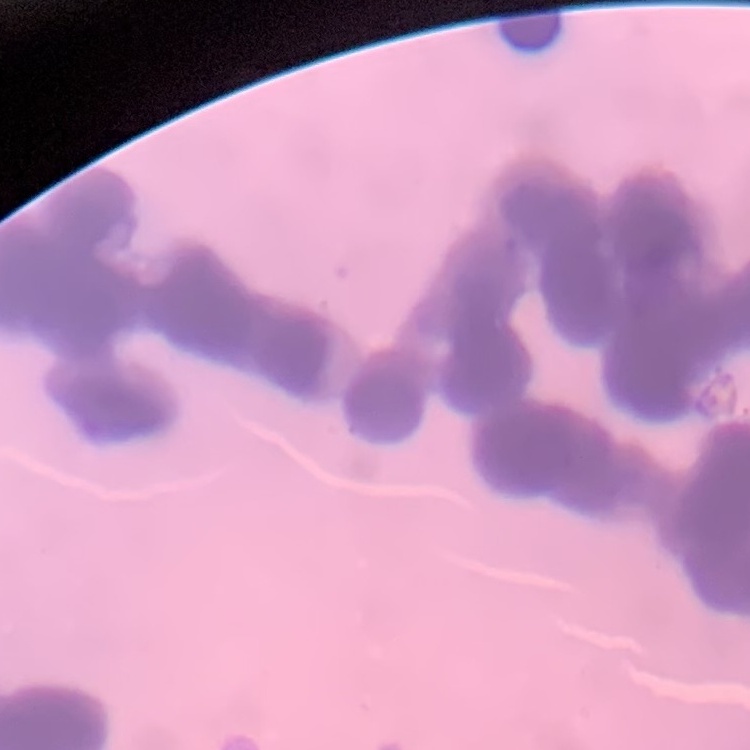
red blood cell morphology = rouleaux formation
image type = one tile cut from a larger photomicrograph
preparation = thin blood film
stain = Field's or Giemsa